Point out each malaria parasite and classify it by life-cycle stage.
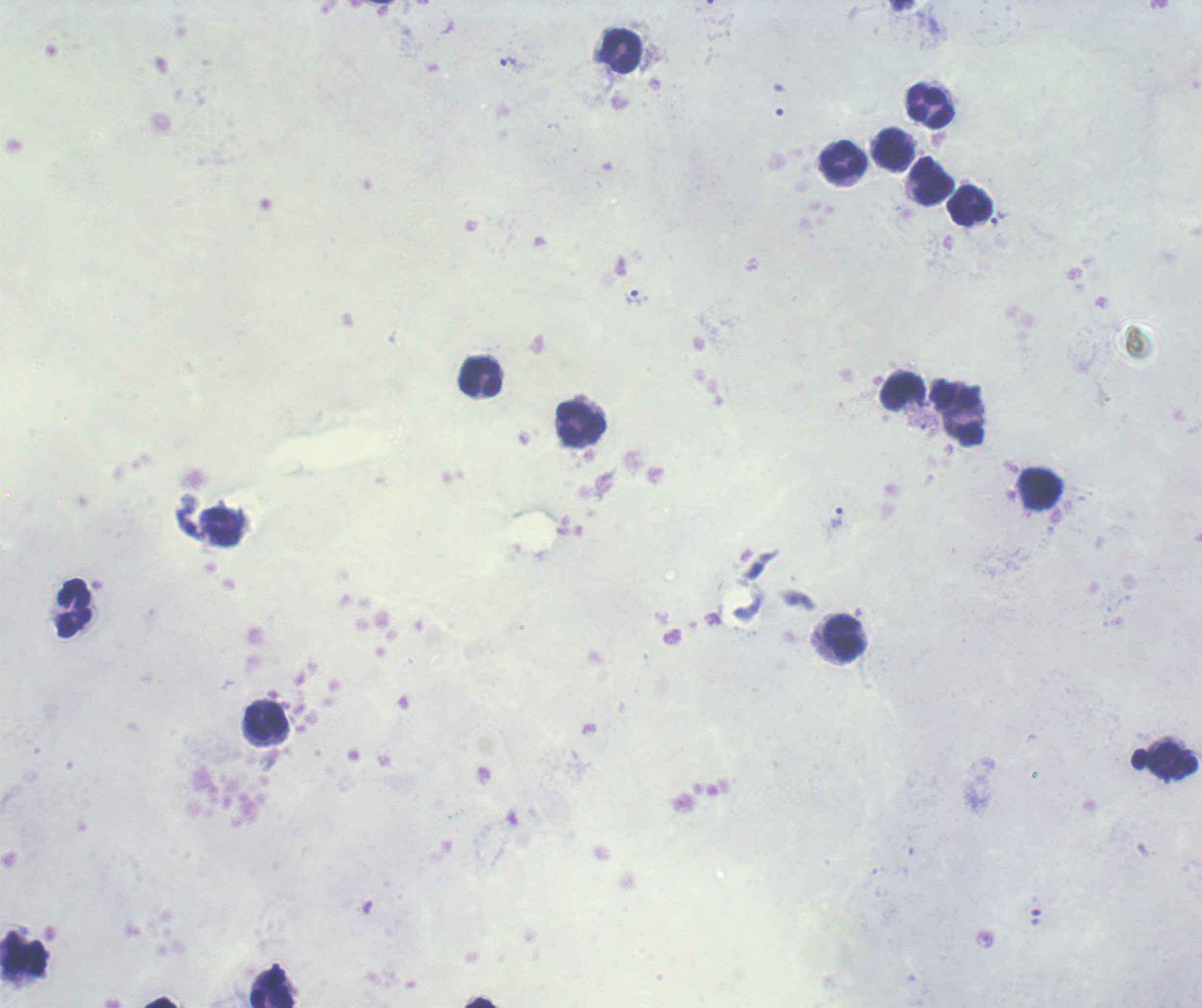
Approximate object centers, in pixels from the top-left corner.
Trophozoites: (x=509, y=62), (x=636, y=298), (x=837, y=517).
No schizont or gametocyte forms observed.

coordinate format = approximate object centers, in pixels from the top-left corner
leukocyte locations = (x=620, y=50), (x=930, y=106), (x=893, y=150), (x=843, y=161), (x=932, y=181), (x=970, y=206), (x=480, y=378), (x=903, y=392), (x=958, y=414), (x=580, y=424), (x=1040, y=490), (x=73, y=608), (x=845, y=638), (x=267, y=720), (x=24, y=955), (x=274, y=989)
image size = 1202×1008 pixels
field of view = single
preparation = thick blood smear
magnification = 100x
context = previously used in a real diagnosis
background quality = poor
stain = Romanowsky